State the preparation type.
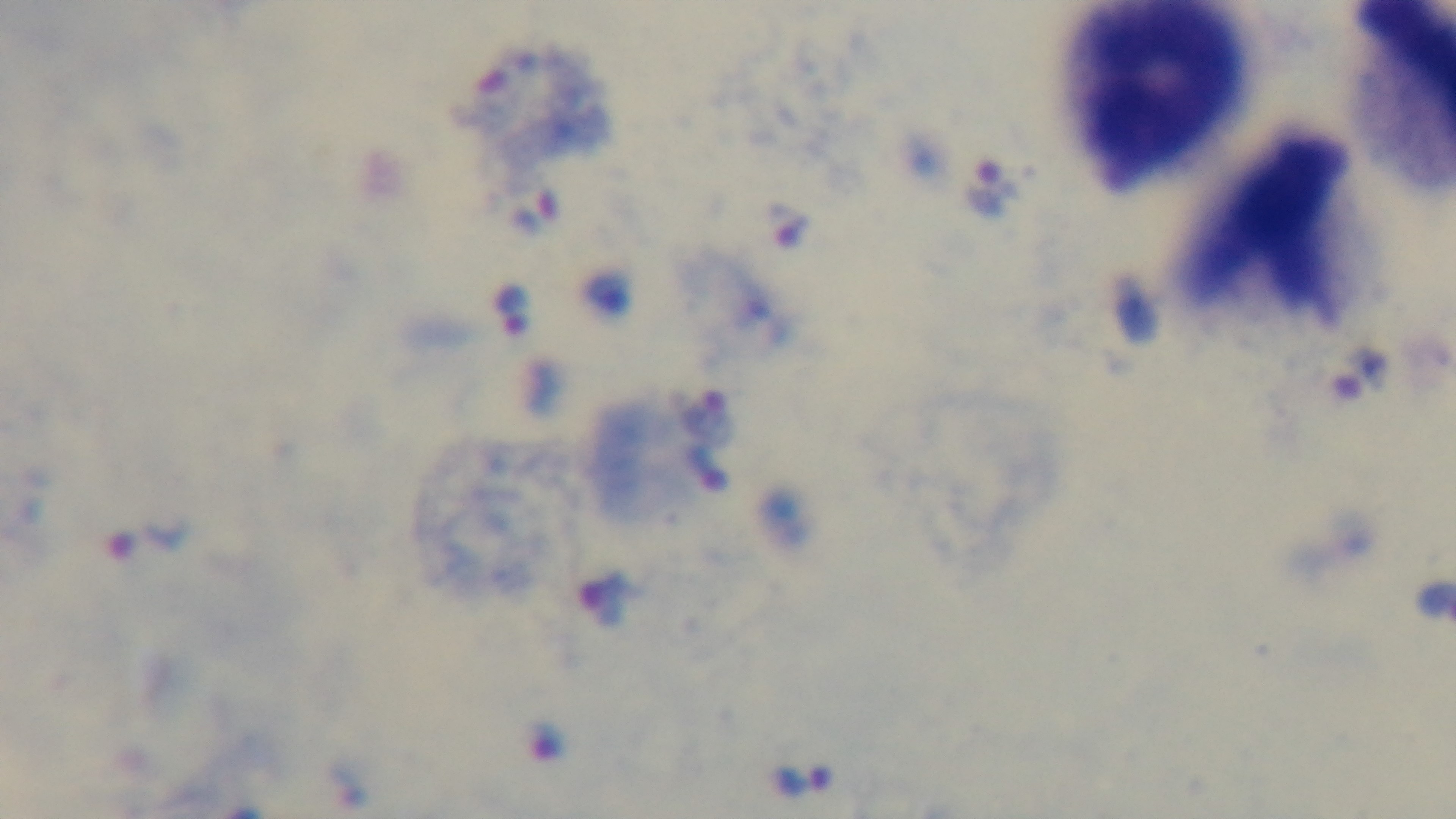
A thick smear.

Summary:
  - Capture: mounted 4K digital camera
  - Malaria status: positive
  - Stain: Giemsa
  - Modality: light microscopy
  - Objective: 100x oil immersion
  - Field of view: single